State which parasite is depicted.
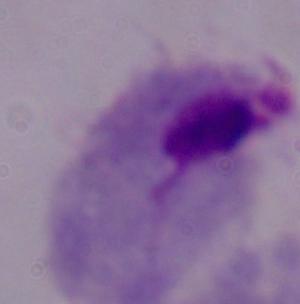
This is a trichomonad.

Summary:
  - Magnification: 1000x
  - Modality: micrograph